Point out Plasmodium parasites and leukocytes.
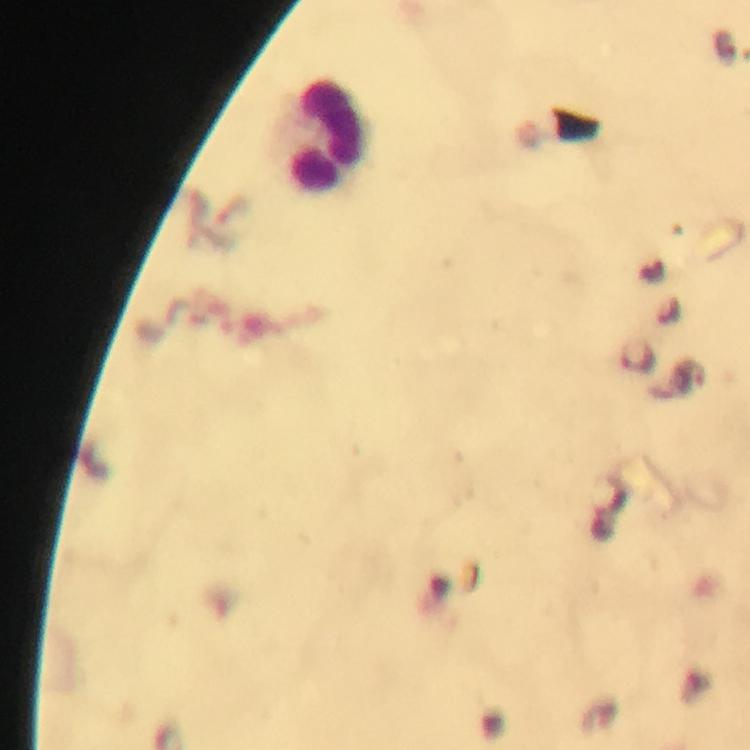

Approximate object centers, in pixels from the top-left corner.
Plasmodium parasites: (x=635, y=355).
Leukocytes: (x=328, y=136).

Giemsa stain. 100x magnification. Photographed with a smartphone mounted on the microscope. A crop from one field of view. Immersion oil was used. From a malaria diagnostic workup. Thick blood smear. Image is 750×750 pixels.